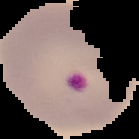
result = malaria parasites identified
preparation = thin blood smear
image size = 139×139 pixels
image type = segmented cell region on a black background